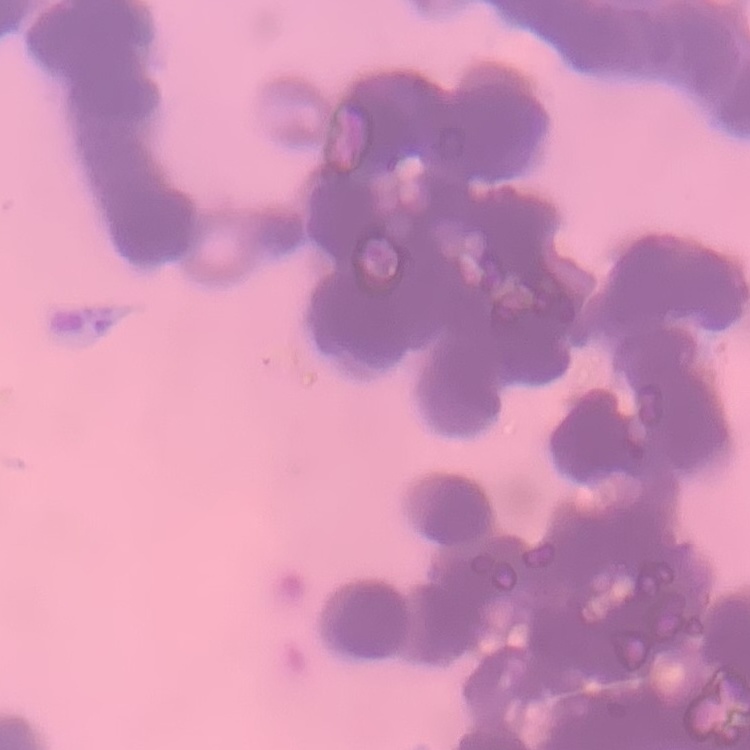
The erythrocytes show rouleaux formation. Thin blood smear. Square crop of a larger photomicrograph. Field's or Giemsa stain.